Assess the background quality.
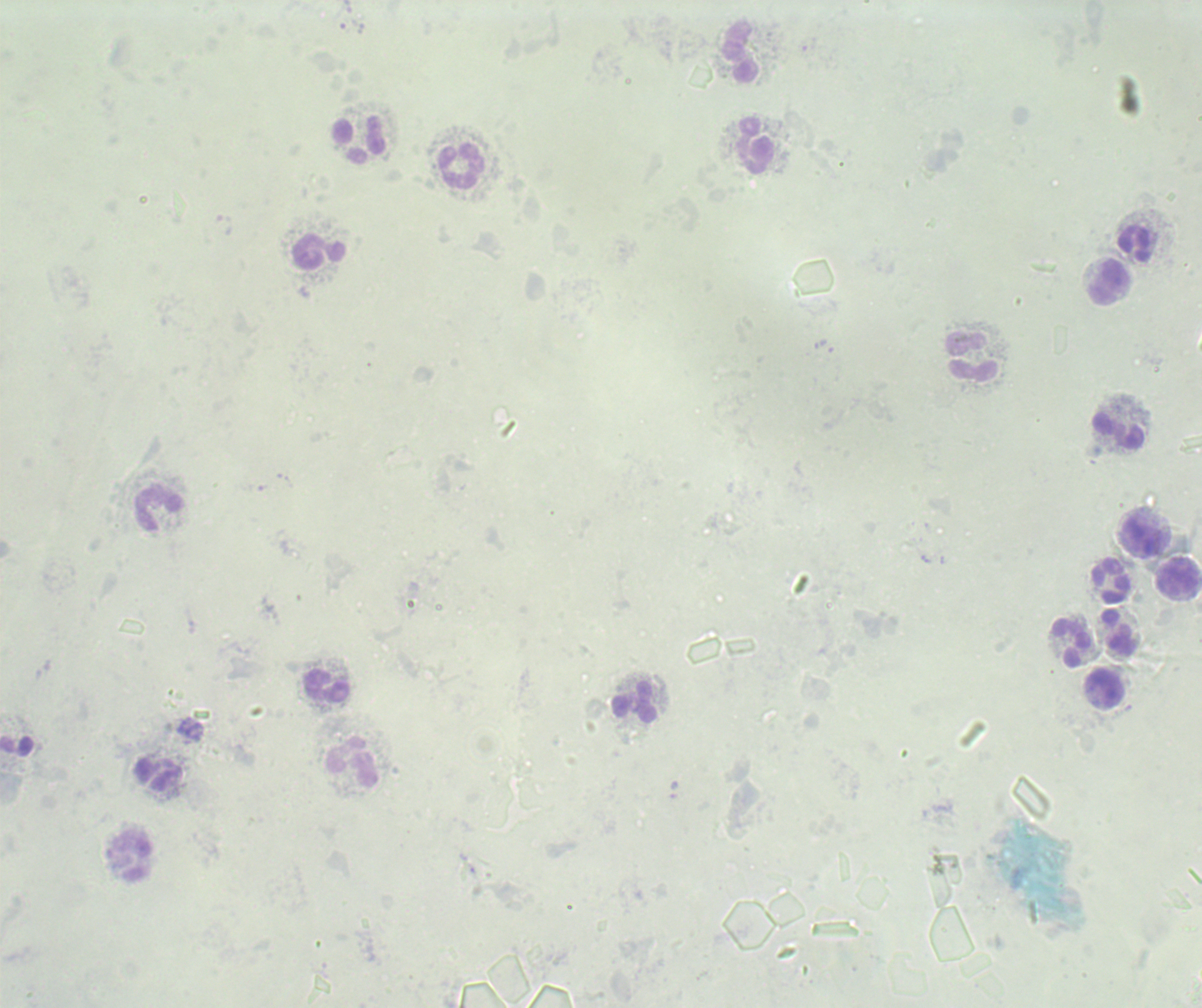

Poor.

coordinate format = approximate centers as (x, y) in pixels
leukocyte locations = (740, 53), (359, 140), (755, 146), (461, 166), (1135, 244), (319, 251), (1109, 282), (974, 357), (1117, 431), (158, 509), (1142, 540), (1177, 578), (1111, 581), (1118, 633), (1071, 643), (327, 687), (1105, 689), (634, 703), (352, 762), (158, 775), (132, 858)
result = no malaria parasites detected
preparation = thick blood smear
context = previously used in an actual diagnosis
magnification = 100x
image size = 1202×1008 pixels
stain = Romanowsky
field of view = single